Assess this cell for malaria.
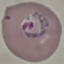
Parasitized.

stain = Giemsa
image type = automatically extracted cell patch, resized to 64 × 64 pixels
capture = smartphone through the microscope eyepiece
preparation = thin blood smear